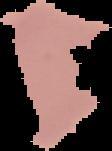 Malaria status: uninfected. From a thin blood smear. Image is 112×151 pixels. Cell region segmented out of the field of view; the surrounding area is masked to black.